Locate and identify every blood parasite.
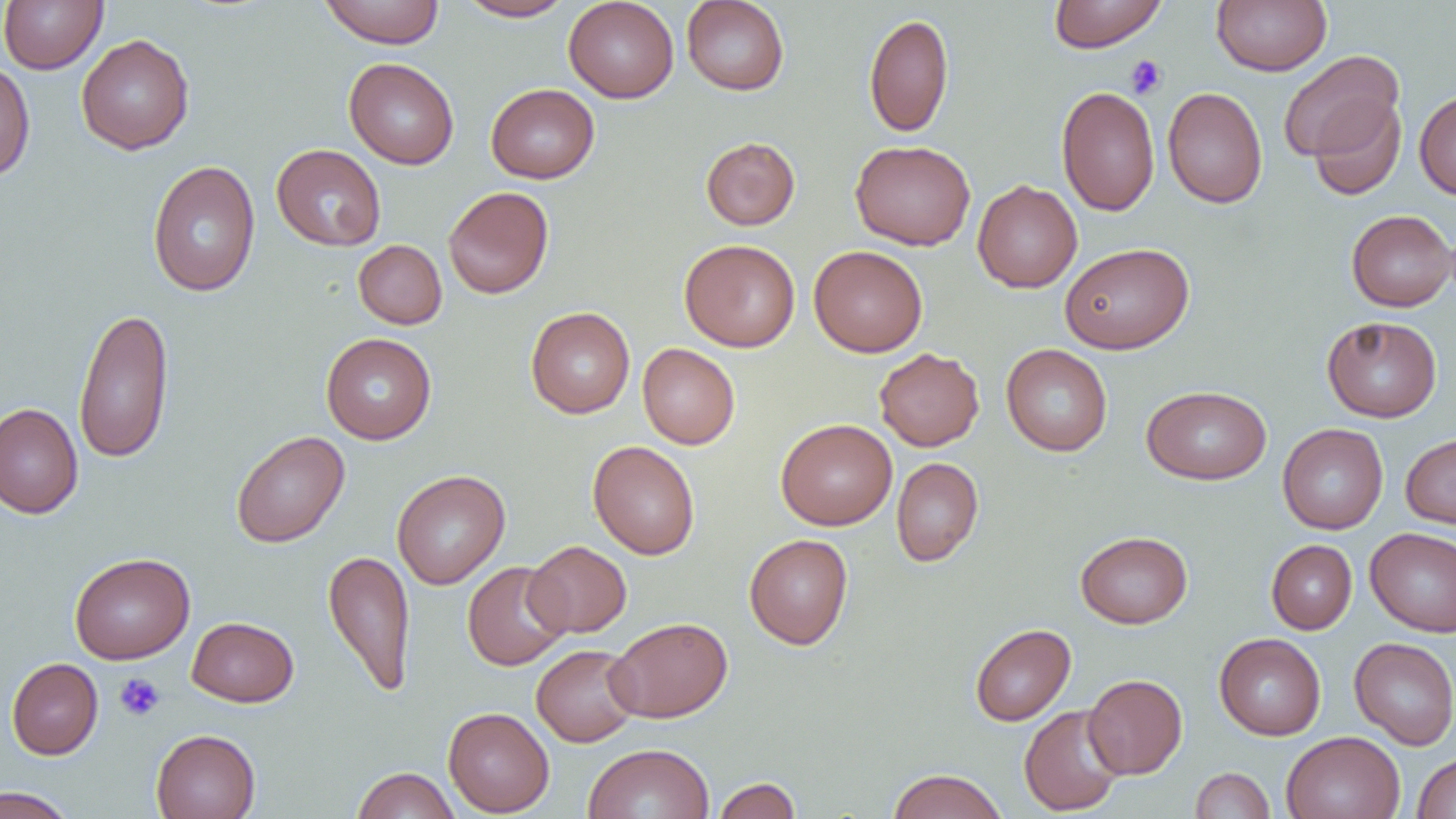

No blood parasites seen.

Approximate bounding boxes as (x1, y1, x2, y2) in pixels. Uninfected red blood cell locations: (0, 0, 107, 74), (319, 0, 445, 48), (456, 0, 574, 21), (564, 0, 679, 103), (1048, 0, 1167, 52), (1212, 0, 1330, 76), (681, 1, 789, 95), (863, 12, 954, 138), (76, 34, 195, 154), (1278, 49, 1404, 163), (344, 57, 459, 169), (0, 61, 36, 182), (486, 83, 599, 183), (1057, 85, 1159, 216), (1162, 87, 1267, 208), (1414, 90, 1456, 200), (1306, 96, 1407, 200), (700, 136, 800, 230), (850, 140, 976, 250), (271, 144, 386, 251), (147, 160, 261, 297), (972, 180, 1082, 293), (443, 186, 554, 299), (1346, 209, 1455, 312), (353, 239, 447, 329), (679, 239, 801, 352), (1060, 242, 1194, 354), (809, 245, 928, 357), (73, 306, 174, 464), (525, 306, 636, 418), (1322, 316, 1442, 422), (321, 332, 436, 444), (637, 343, 740, 449), (1001, 343, 1112, 456), (874, 347, 984, 451), (1141, 384, 1272, 484), (0, 402, 83, 518), (775, 418, 897, 530), (1278, 423, 1388, 534), (230, 430, 350, 548), (1400, 433, 1456, 531), (588, 440, 700, 559), (891, 456, 984, 567), (391, 470, 510, 589), (1366, 527, 1456, 636), (1075, 530, 1192, 628), (744, 534, 853, 650), (1266, 539, 1357, 634), (525, 540, 632, 637), (323, 549, 416, 697), (69, 552, 195, 664), (462, 561, 571, 670), (187, 616, 299, 707), (606, 616, 733, 723), (970, 623, 1076, 726), (1214, 633, 1326, 740), (1349, 637, 1456, 750), (531, 644, 641, 747), (7, 657, 103, 759), (1082, 674, 1187, 779), (1019, 704, 1126, 816), (443, 707, 555, 816), (151, 728, 261, 819), (1281, 731, 1405, 819), (583, 742, 714, 819), (1411, 752, 1456, 818), (351, 766, 461, 819), (1190, 767, 1275, 819), (887, 768, 1008, 819), (712, 776, 802, 819), (0, 786, 77, 819). Platelet locations: (1125, 54, 1167, 99), (114, 673, 166, 721). Slide-level diagnosis: negative for blood parasites. Image is 1456×819 pixels. Optical microscopy. Captured at 1000x magnification. Thin blood film. One field of a larger specimen.